Report the malaria status of this cell.
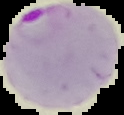

Parasitized.

image_type: cell region segmented out of the field of view; surrounding area masked to black
image_size: 124×115 pixels
preparation: thin blood film